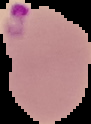
Result: malaria parasites detected. Cell region segmented out of the field of view; the surrounding area is masked to black. From a thin blood film. Image is 91×124 pixels.